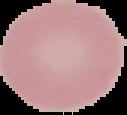

image type = segmented cell region on a black background
image size = 127×115 pixels
preparation = thin blood film
malaria status = uninfected